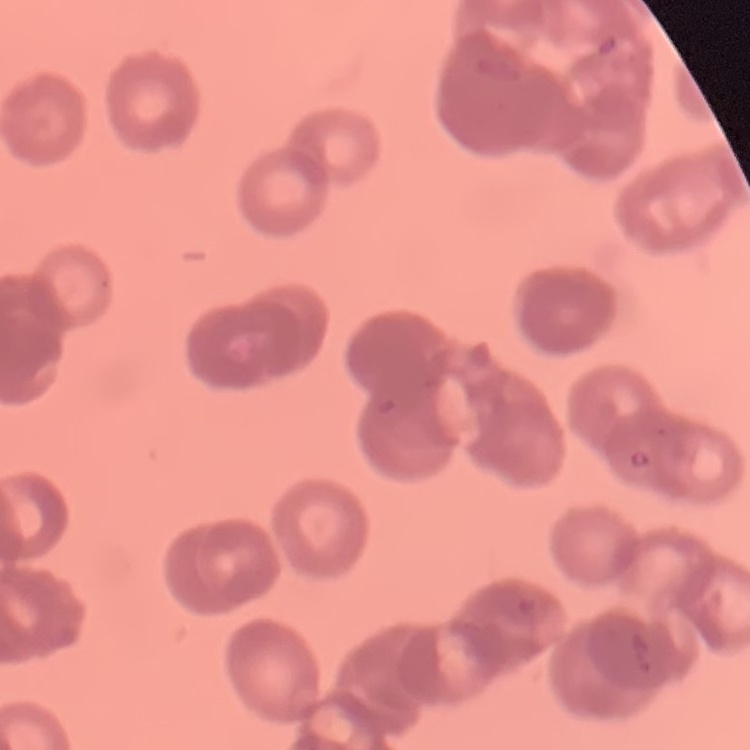
Summary:
  - Erythrocyte morphology: rouleaux formation
  - Preparation: thin peripheral smear
  - Stain: Field's or Giemsa
  - Image type: square crop of a larger photomicrograph